Outline each blood parasite and name the species.
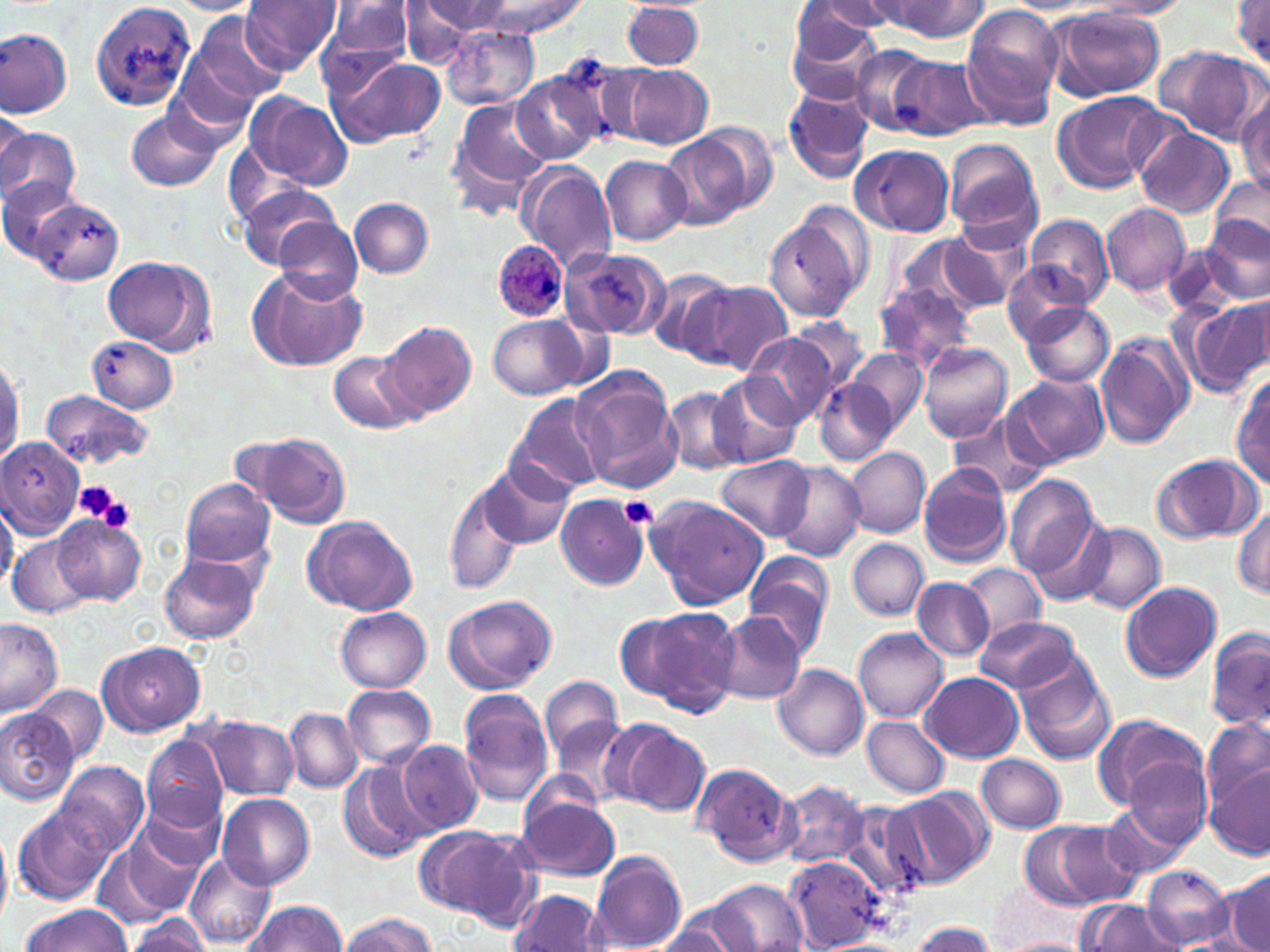
Approximate bounding boxes as (x1, y1, x2, y2) in pixels.
Plasmodium ovale-infected red blood cells: (492, 242, 570, 320).
No Plasmodium falciparum, Plasmodium malariae, Plasmodium vivax, Babesia divergens, or Trypanosoma brucei observed.

Summary:
  - Uninfected red blood cell locations: (88, 0, 197, 107), (240, 0, 341, 73), (325, 0, 415, 64), (419, 0, 511, 39), (872, 0, 988, 41), (1082, 0, 1192, 18), (1233, 0, 1269, 67), (169, 1, 264, 15), (482, 1, 585, 37), (812, 1, 913, 33), (622, 3, 704, 70), (398, 4, 477, 67), (795, 4, 894, 55), (960, 7, 1062, 129), (1048, 7, 1167, 102), (786, 12, 884, 104), (187, 13, 288, 110), (313, 17, 413, 97), (444, 26, 540, 109), (1, 29, 72, 119), (852, 45, 936, 137), (1157, 46, 1266, 144), (327, 55, 446, 149), (558, 55, 660, 146), (890, 55, 990, 141), (618, 63, 712, 148), (510, 71, 604, 164), (783, 84, 874, 184), (1051, 91, 1166, 192), (244, 92, 352, 190), (1236, 95, 1270, 197), (445, 97, 552, 216), (127, 108, 223, 192), (0, 114, 37, 194), (694, 123, 780, 215), (0, 125, 83, 208), (1134, 127, 1234, 217), (666, 135, 751, 231), (943, 139, 1042, 243), (850, 144, 954, 237), (601, 154, 691, 245), (516, 160, 619, 274), (0, 176, 84, 261), (1209, 177, 1268, 254), (238, 184, 344, 271), (349, 198, 434, 278), (30, 199, 124, 285), (1102, 203, 1190, 297), (764, 213, 866, 323), (1027, 214, 1112, 306), (1199, 216, 1270, 305), (274, 218, 364, 305), (939, 223, 1032, 312), (895, 235, 986, 315), (1163, 244, 1243, 316), (561, 247, 670, 341), (103, 255, 215, 353), (1001, 264, 1083, 344), (247, 266, 367, 374), (646, 269, 734, 360), (697, 282, 793, 374), (872, 283, 977, 373), (1183, 299, 1270, 395), (1022, 303, 1114, 388), (489, 315, 586, 400), (780, 316, 869, 409), (377, 321, 477, 421), (746, 332, 841, 427), (1095, 333, 1194, 449), (87, 335, 177, 413), (918, 343, 1011, 442), (847, 347, 927, 434), (0, 348, 23, 467), (329, 350, 420, 434), (572, 370, 680, 487), (710, 372, 803, 469), (1232, 372, 1269, 488), (1006, 374, 1111, 468), (814, 378, 893, 466), (663, 387, 746, 476), (40, 390, 154, 470), (506, 393, 609, 499), (948, 409, 1054, 500), (245, 432, 351, 528), (1, 437, 84, 540), (846, 447, 930, 538), (1151, 454, 1259, 543), (716, 455, 812, 542), (774, 462, 866, 562), (476, 464, 572, 551), (918, 464, 1012, 568), (1005, 476, 1102, 582), (181, 478, 276, 568), (445, 481, 522, 596), (557, 495, 647, 589), (647, 495, 768, 610), (0, 502, 19, 589), (1233, 507, 1269, 597), (54, 515, 147, 606), (302, 515, 417, 615), (1077, 522, 1166, 614), (7, 533, 91, 619), (847, 538, 929, 620), (742, 550, 833, 653), (158, 551, 263, 644), (960, 565, 1046, 646), (913, 577, 994, 661), (1120, 581, 1221, 682), (445, 594, 557, 693), (631, 606, 739, 714), (335, 608, 432, 692), (717, 614, 805, 704), (976, 616, 1078, 694), (0, 617, 63, 717), (1206, 625, 1270, 734), (853, 628, 947, 721), (97, 639, 205, 737), (1013, 651, 1115, 766), (773, 664, 868, 759), (921, 672, 1023, 762), (538, 674, 623, 763), (341, 684, 436, 769), (29, 685, 107, 764), (457, 690, 555, 807), (284, 708, 362, 793), (0, 710, 78, 806), (199, 713, 299, 801), (1095, 714, 1206, 811), (862, 715, 951, 798), (552, 716, 632, 805), (1203, 717, 1269, 809), (613, 723, 711, 815), (140, 733, 228, 832), (398, 739, 483, 832), (978, 754, 1066, 833), (1121, 755, 1211, 850), (57, 760, 151, 856), (694, 761, 800, 866), (1204, 761, 1270, 860), (338, 762, 434, 862), (775, 781, 868, 868), (887, 788, 992, 889), (137, 789, 231, 874), (217, 794, 315, 890), (519, 794, 621, 881), (840, 800, 926, 899), (13, 803, 114, 904), (1103, 807, 1188, 881), (122, 817, 214, 916), (1037, 821, 1144, 908), (414, 826, 528, 920), (592, 850, 687, 949), (184, 852, 276, 949), (786, 854, 884, 952), (1142, 866, 1232, 947), (1225, 867, 1270, 952), (703, 880, 806, 952), (509, 890, 608, 951), (242, 900, 350, 952), (1079, 900, 1181, 952), (18, 903, 130, 952), (338, 912, 437, 951), (126, 914, 213, 951), (650, 914, 740, 952), (908, 921, 997, 952), (998, 936, 1091, 952)
  - Platelet locations: (74, 478, 124, 524), (94, 492, 136, 535), (619, 495, 658, 530)
  - Slide-level diagnosis: Plasmodium ovale
  - Stain: May-Grünwald-Giemsa
  - Field of view: single
  - Magnification: 1000x
  - Modality: optical microscopy
  - Image size: 1270×952 pixels
  - Preparation: thin blood film